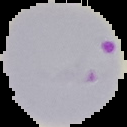 Image is 127×127 pixels. From a thin blood smear. Malaria status: parasitized. The area outside the segmented cell region is set to black.